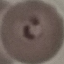
malaria status = parasitized
capture = smartphone camera at the microscope eyepiece
image type = automatically extracted cell patch, resized to 64 × 64 pixels
stain = Giemsa
preparation = thin blood film